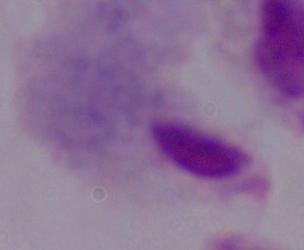 1000x magnification. A trichomonad is shown. Micrograph.